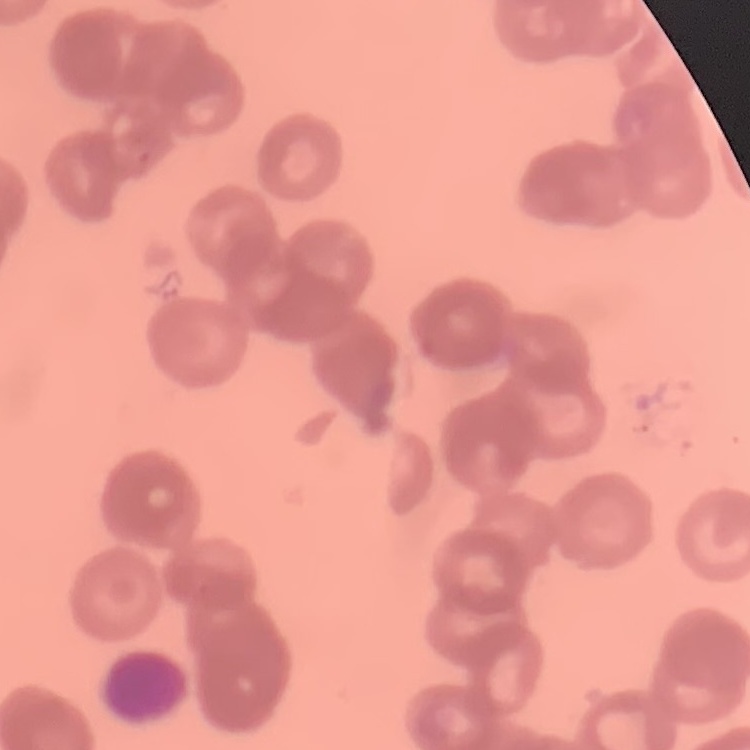

red blood cell morphology = rouleaux formation
preparation = thin blood film
stain = Field's or Giemsa
image type = one tile cut from a larger photomicrograph